Assess this cell for malaria.
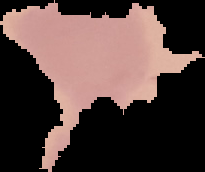

It is uninfected.

The area outside the segmented cell region is set to black. From a thin blood smear. Image is 205×172 pixels.